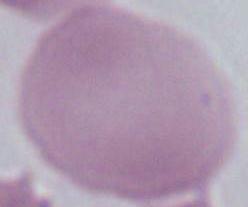 Captured at 1000x magnification. An erythrocyte is shown. Photomicrograph.